Classify this cell by malaria status.
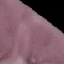
Uninfected.

{
  "capture": "smartphone through the microscope eyepiece",
  "image_type": "automatically extracted cell patch, resized to 64 × 64 pixels",
  "preparation": "thin blood smear",
  "stain": "Giemsa"
}